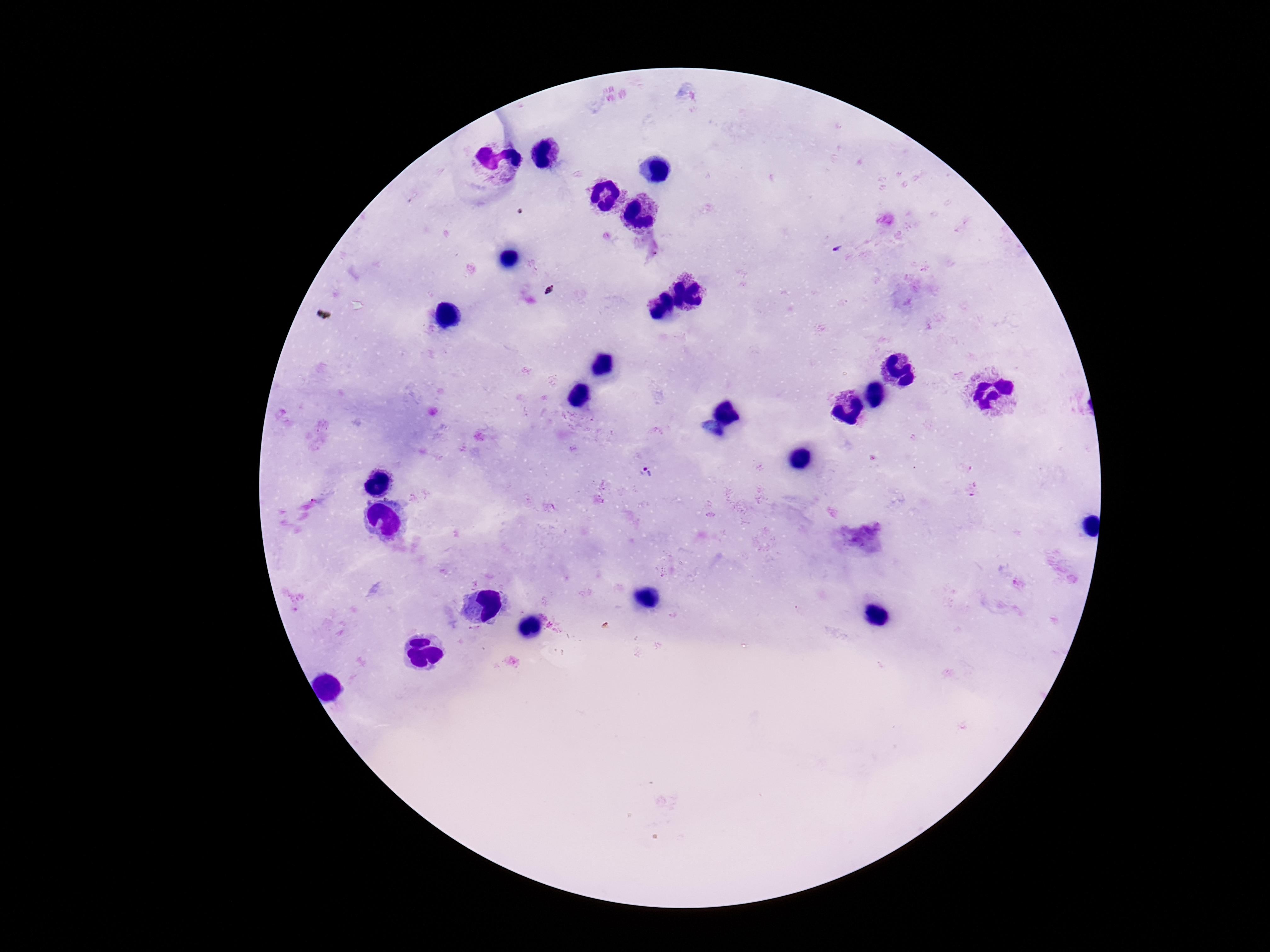
Approximate object centers, in pixels from the top-left corner. Plasmodium parasite locations: (x=648, y=473). Single field of view. Giemsa-stained preparation. Image is 1270×952 pixels. Patient malaria status: infected. Smartphone photograph taken through the microscope eyepiece. Thick blood film. 100x magnification.